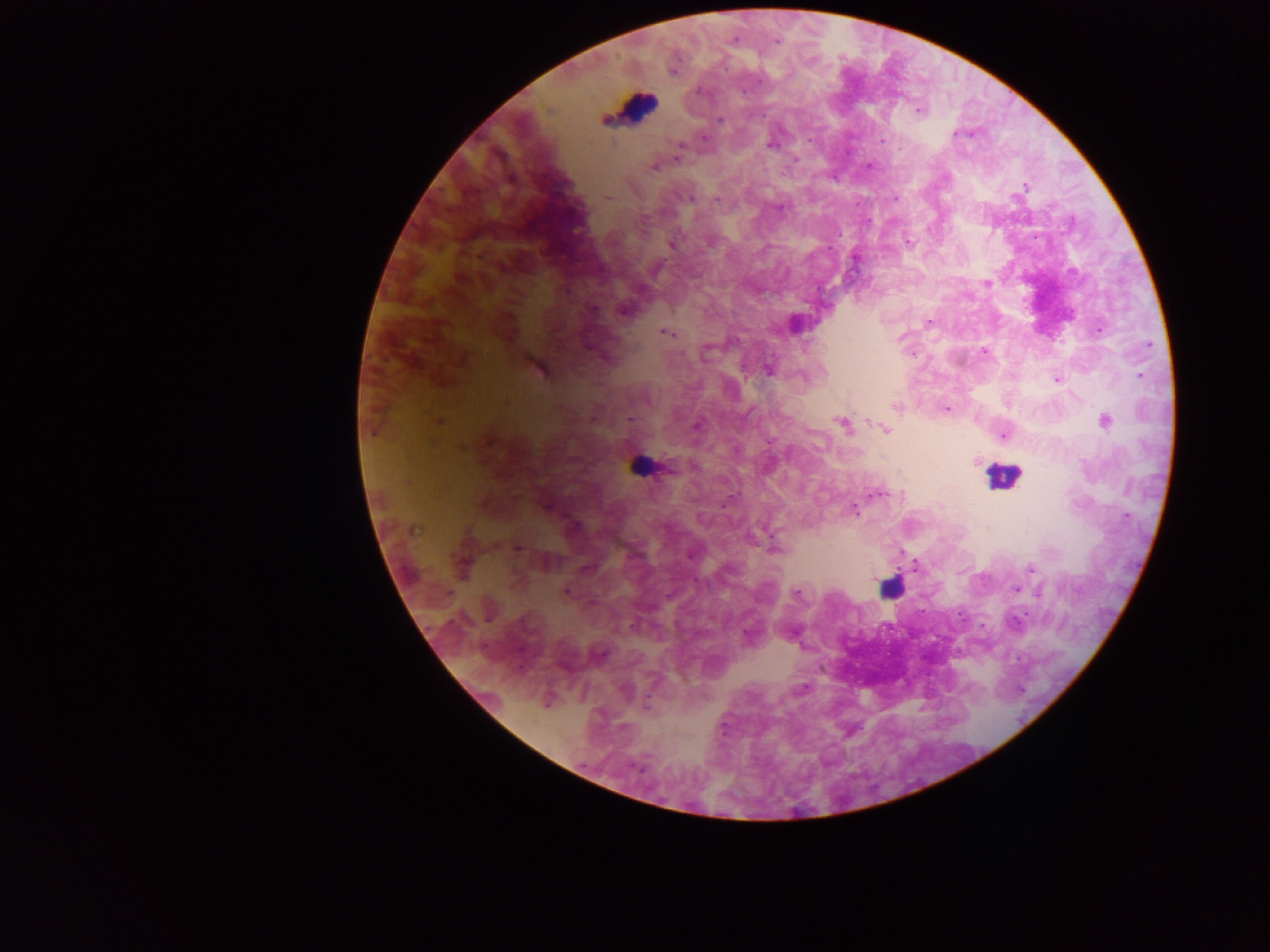
field_of_view: single
country: Ghana
preparation: thick blood film
capture: mobile-phone photograph through a microscope
plasmodium_parasite_locations: 'approximate centers as (x, y) in pixels: (776, 41), (919, 110), (720, 120), (702, 137), (772, 142), (679, 149), (677, 158), (794, 159), (870, 164), (653, 166), (1025, 185), (606, 197), (692, 198), (894, 198), (716, 199), (907, 242), (671, 244), (854, 257), (987, 282), (623, 310), (928, 322), (794, 324), (664, 332), (901, 337), (984, 351), (535, 366), (767, 369), (1140, 375), (1056, 379), (896, 406), (946, 408), (437, 421), (1105, 421), (696, 424), (842, 424), (885, 429), (1004, 434), (487, 439), (975, 461), (875, 493), (855, 510), (517, 547), (773, 550), (901, 552), (1031, 568), (1016, 589), (564, 592), (796, 593)'
leukocyte_locations: 'approximate centers as (x, y) in pixels: (633, 107), (639, 465), (1003, 476), (889, 587)'
image_size: 1270×952 pixels